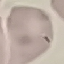
Malaria status: uninfected. Giemsa-stained preparation. Automatically extracted cell patch, resized to 64 × 64 pixels. Thin blood smear. Acquired by smartphone through the microscope eyepiece.